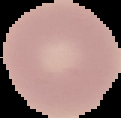 Image is 121×118 pixels. Result: no malaria parasites detected. Segmented cell region on a black background. From a thin blood smear.